Name the parasite shown.
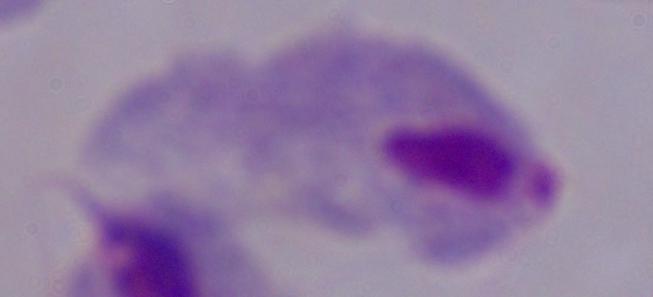

A trichomonad.

Summary:
  - Modality: photomicrograph
  - Magnification: 1000x